State which parasite is depicted.
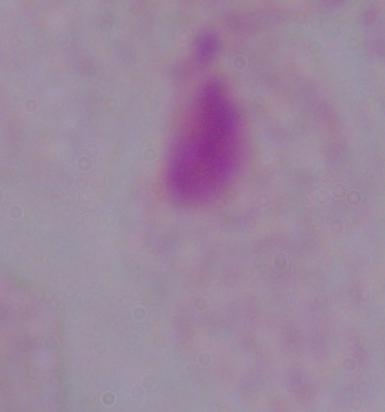
This is a trichomonad.

Summary:
  - Modality: photomicrograph
  - Magnification: 1000x